Locate and identify every blood parasite.
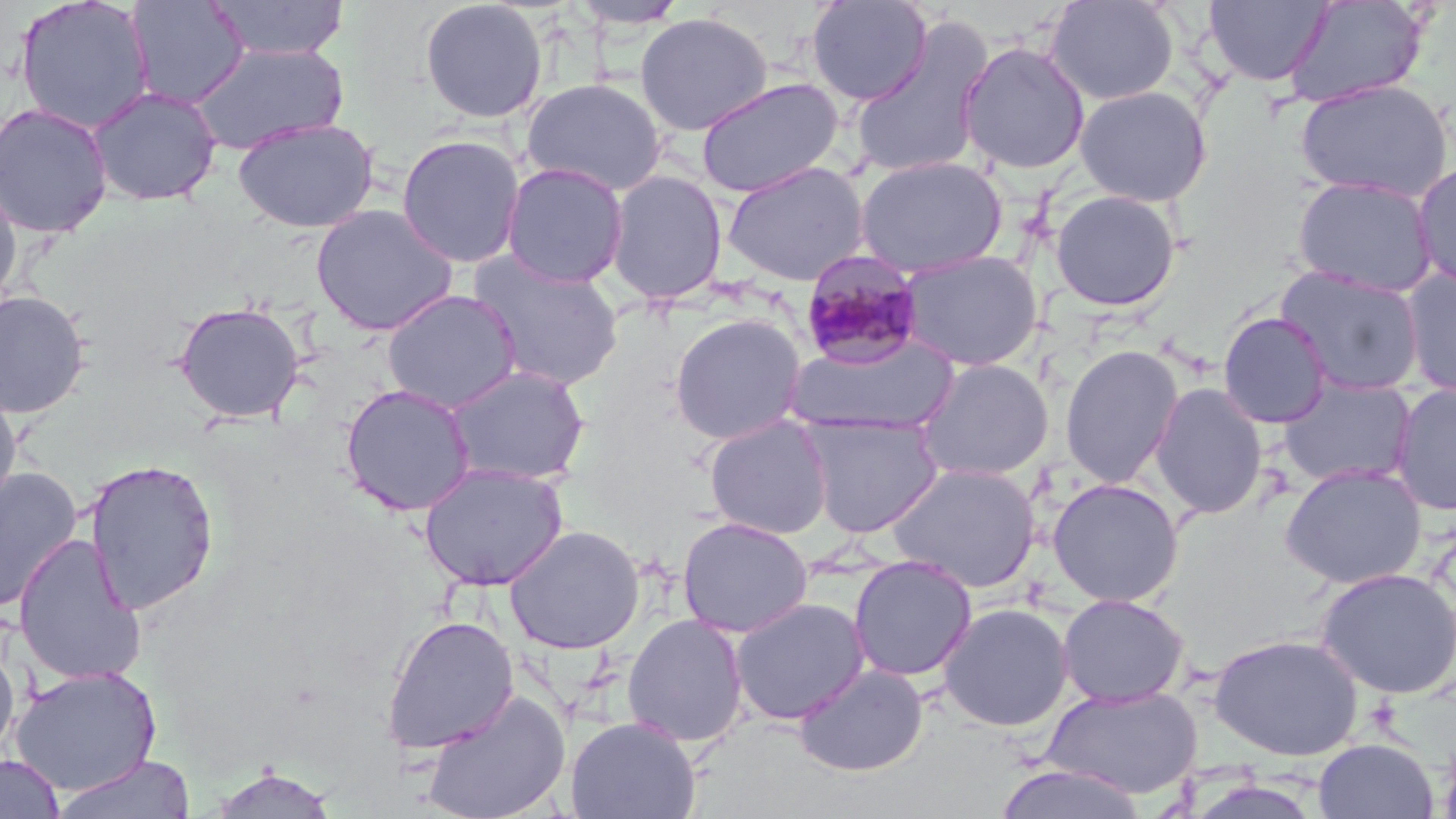

Approximate bounding boxes as [x1, y1, x2, y2] in pixels.
Plasmodium malariae-infected red blood cells: [800, 250, 926, 369].
No Plasmodium falciparum, Plasmodium ovale, Plasmodium vivax, Babesia divergens, or Trypanosoma brucei observed.

Summary:
  - Uninfected red blood cell locations: [14, 0, 156, 134], [205, 0, 350, 61], [806, 0, 933, 106], [1044, 0, 1179, 106], [126, 1, 249, 110], [419, 1, 548, 124], [567, 1, 690, 30], [1203, 1, 1333, 87], [1284, 1, 1429, 108], [634, 12, 773, 136], [851, 18, 994, 181], [957, 41, 1091, 175], [189, 42, 349, 153], [520, 76, 668, 197], [695, 77, 845, 198], [1295, 78, 1453, 201], [1075, 85, 1212, 206], [87, 86, 222, 207], [0, 101, 114, 238], [232, 117, 380, 233], [396, 134, 525, 269], [855, 155, 1008, 278], [722, 161, 869, 286], [1412, 161, 1456, 290], [501, 162, 629, 289], [605, 169, 728, 305], [1292, 176, 1439, 297], [0, 179, 23, 314], [1049, 189, 1182, 312], [310, 203, 460, 336], [898, 250, 1043, 371], [465, 251, 625, 391], [1275, 266, 1426, 396], [1399, 267, 1456, 399], [382, 289, 521, 413], [0, 290, 92, 419], [173, 300, 305, 424], [1218, 311, 1333, 429], [670, 313, 806, 445], [784, 334, 961, 436], [1059, 344, 1184, 488], [915, 358, 1054, 481], [444, 364, 590, 486], [1278, 376, 1417, 488], [1390, 382, 1456, 516], [340, 383, 476, 516], [1150, 383, 1268, 520], [0, 386, 22, 519], [800, 413, 943, 537], [703, 415, 833, 539], [83, 458, 219, 616], [419, 462, 568, 590], [887, 462, 1041, 593], [1279, 463, 1427, 589], [0, 467, 83, 612], [1047, 477, 1184, 606], [677, 516, 813, 638], [504, 524, 645, 653], [13, 533, 147, 685], [848, 555, 977, 682], [1315, 567, 1456, 698], [1057, 593, 1190, 707], [729, 597, 869, 726], [938, 602, 1073, 731], [381, 613, 520, 754], [623, 613, 748, 748], [1209, 633, 1364, 761], [0, 635, 20, 762], [794, 663, 928, 777], [10, 665, 162, 797], [1042, 684, 1203, 799], [420, 688, 572, 819], [566, 715, 701, 819], [1313, 737, 1438, 819], [52, 753, 197, 819], [0, 754, 65, 818], [995, 762, 1148, 819], [206, 766, 339, 818]
  - Slide-level diagnosis: Plasmodium malariae
  - Field of view: single
  - Magnification: 1000x
  - Stain: May-Grünwald-Giemsa
  - Preparation: thin blood film
  - Modality: optical microscopy
  - Image size: 1456×819 pixels